Locate every malaria parasite and every leukocyte.
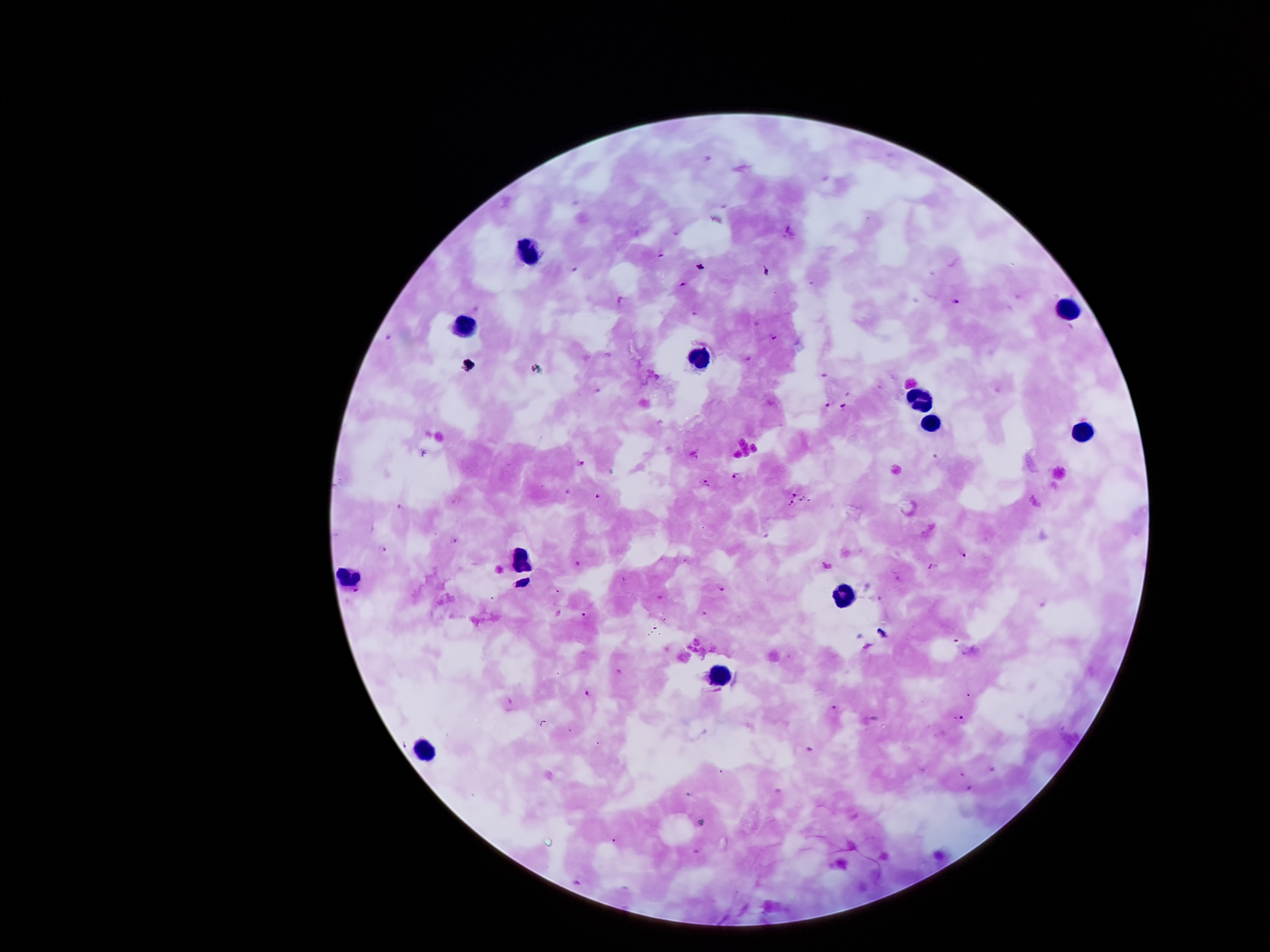
Approximate centers as [x, y] in pixels.
Malaria parasites: [662, 253], [684, 285], [956, 300], [773, 336], [828, 405], [843, 406], [581, 464], [733, 475], [706, 483], [796, 492], [597, 495], [801, 499], [790, 503], [454, 542], [384, 547], [963, 555], [578, 564], [932, 566], [722, 588], [589, 614], [589, 693], [836, 709], [963, 720].
Leukocytes: [528, 252], [1070, 302], [463, 323], [700, 360], [918, 403], [931, 425], [1085, 431], [519, 558], [346, 572], [843, 593], [720, 676], [427, 747].

Summary:
  - Stain: Giemsa
  - Capture: smartphone through the microscope eyepiece
  - Preparation: thick blood film
  - Magnification: 100x
  - Field of view: one from this slide
  - Patient malaria status: positive for Plasmodium falciparum
  - Image size: 1270×952 pixels